Name the parasite shown.
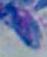

Toxoplasma gondii.

magnification = 1000x
modality = photomicrograph